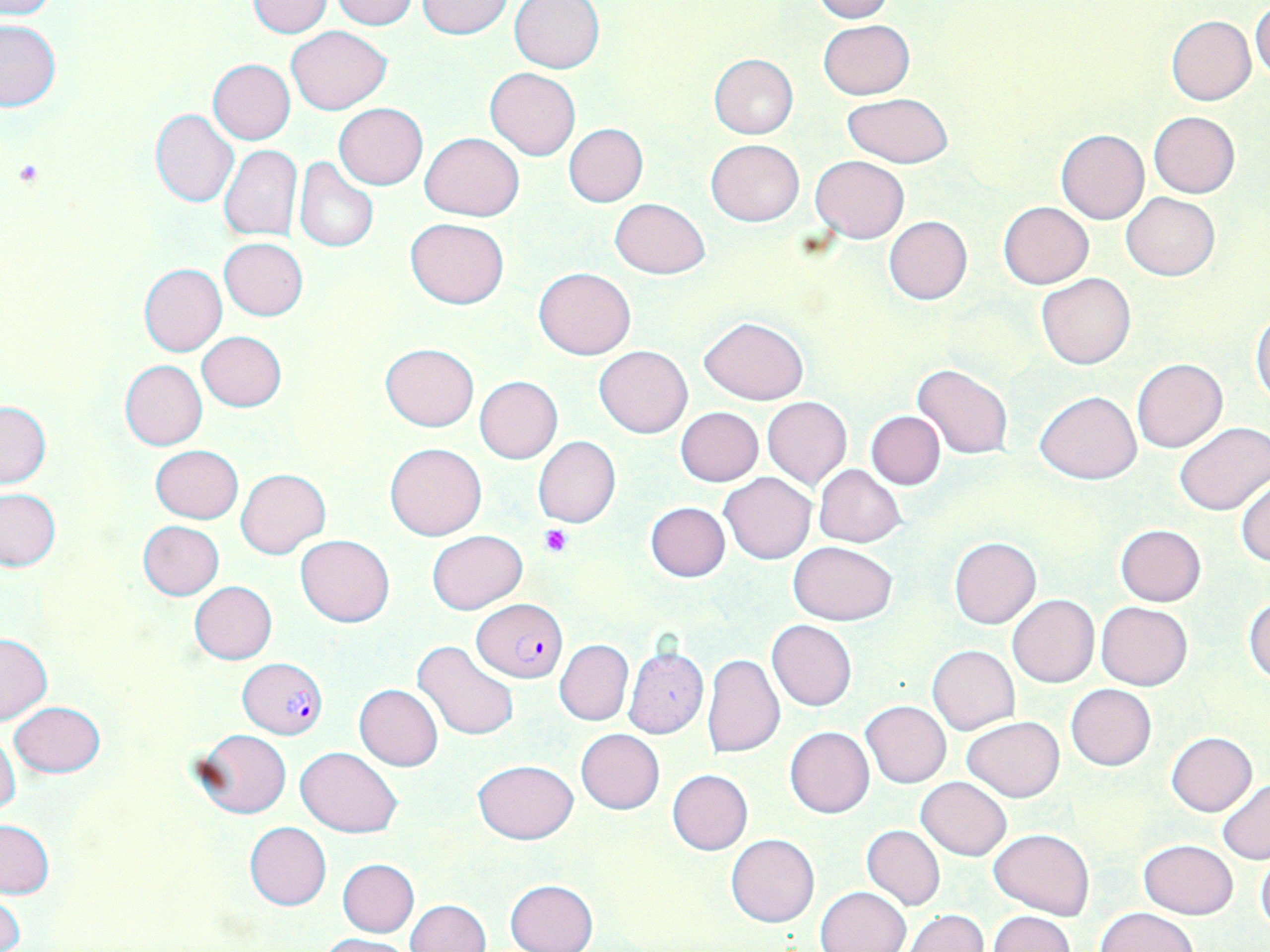

slide-level diagnosis = Plasmodium falciparum
field of view = single
magnification = 1000x
modality = light microscopy
Plasmodium falciparum-infected red blood cell locations = approximate bounding boxes as [x1, y1, x2, y2] in pixels: [472, 599, 568, 683], [239, 659, 324, 737]
platelet locations = approximate bounding boxes as [x1, y1, x2, y2] in pixels: [539, 524, 575, 558]
image size = 1270×952 pixels
stain = May-Grünwald-Giemsa
uninfected red blood cell locations = approximate bounding boxes as [x1, y1, x2, y2] in pixels: [0, 0, 57, 19], [331, 0, 417, 29], [810, 0, 894, 22], [246, 1, 333, 37], [416, 1, 514, 39], [509, 1, 605, 73], [1250, 4, 1270, 83], [1167, 15, 1256, 105], [819, 19, 913, 98], [0, 20, 62, 112], [286, 26, 391, 114], [708, 53, 798, 138], [208, 59, 295, 144], [485, 68, 581, 160], [842, 94, 954, 167], [334, 104, 428, 189], [150, 108, 239, 208], [1149, 111, 1240, 198], [563, 123, 648, 207], [1055, 129, 1148, 224], [419, 132, 525, 221], [705, 139, 804, 226], [219, 145, 302, 242], [810, 155, 909, 243], [293, 157, 379, 254], [1121, 193, 1220, 280], [609, 198, 711, 278], [997, 201, 1094, 289], [884, 216, 972, 304], [406, 217, 508, 309], [219, 238, 307, 320], [138, 264, 226, 357], [534, 267, 635, 359], [1036, 273, 1135, 370], [1251, 311, 1270, 405], [699, 315, 807, 404], [197, 332, 287, 411], [380, 342, 479, 431], [594, 346, 693, 438], [1132, 358, 1227, 453], [119, 360, 207, 450], [912, 364, 1014, 458], [474, 375, 563, 463], [1035, 390, 1141, 484], [762, 397, 852, 489], [0, 401, 50, 488], [676, 407, 763, 486], [865, 411, 945, 489], [1174, 422, 1269, 515], [532, 435, 620, 528], [385, 442, 487, 541], [150, 445, 242, 523], [814, 465, 906, 547], [236, 468, 330, 558], [720, 472, 815, 564], [1235, 474, 1270, 567], [0, 489, 61, 571], [645, 502, 730, 581], [136, 520, 224, 600], [1115, 524, 1206, 606], [428, 531, 526, 613], [296, 534, 394, 627], [949, 538, 1041, 629], [789, 541, 897, 625], [190, 581, 277, 664], [1006, 593, 1099, 687], [1244, 595, 1270, 684], [1097, 602, 1192, 690], [767, 620, 857, 711], [0, 633, 52, 725], [412, 640, 519, 741], [554, 640, 632, 725], [927, 645, 1019, 734], [623, 646, 708, 738], [700, 653, 784, 757], [1065, 683, 1157, 771], [354, 684, 444, 771], [861, 700, 951, 788], [10, 701, 105, 777], [962, 716, 1064, 802], [784, 727, 874, 818], [194, 728, 291, 818], [575, 728, 664, 814], [0, 731, 21, 818], [1166, 732, 1257, 816], [296, 747, 402, 836], [473, 760, 579, 844], [668, 769, 752, 854], [917, 776, 1011, 860], [1067, 778, 1151, 866], [1217, 778, 1270, 865], [0, 821, 53, 898], [244, 822, 331, 910], [861, 826, 945, 910], [989, 829, 1094, 919], [727, 833, 819, 927], [1138, 839, 1238, 919], [1256, 853, 1269, 934], [337, 859, 419, 937], [505, 879, 598, 952], [815, 886, 911, 952], [2, 892, 24, 952], [406, 900, 492, 952], [1096, 907, 1198, 952], [903, 910, 987, 952], [988, 910, 1076, 952], [318, 934, 412, 952]
preparation = thin blood smear